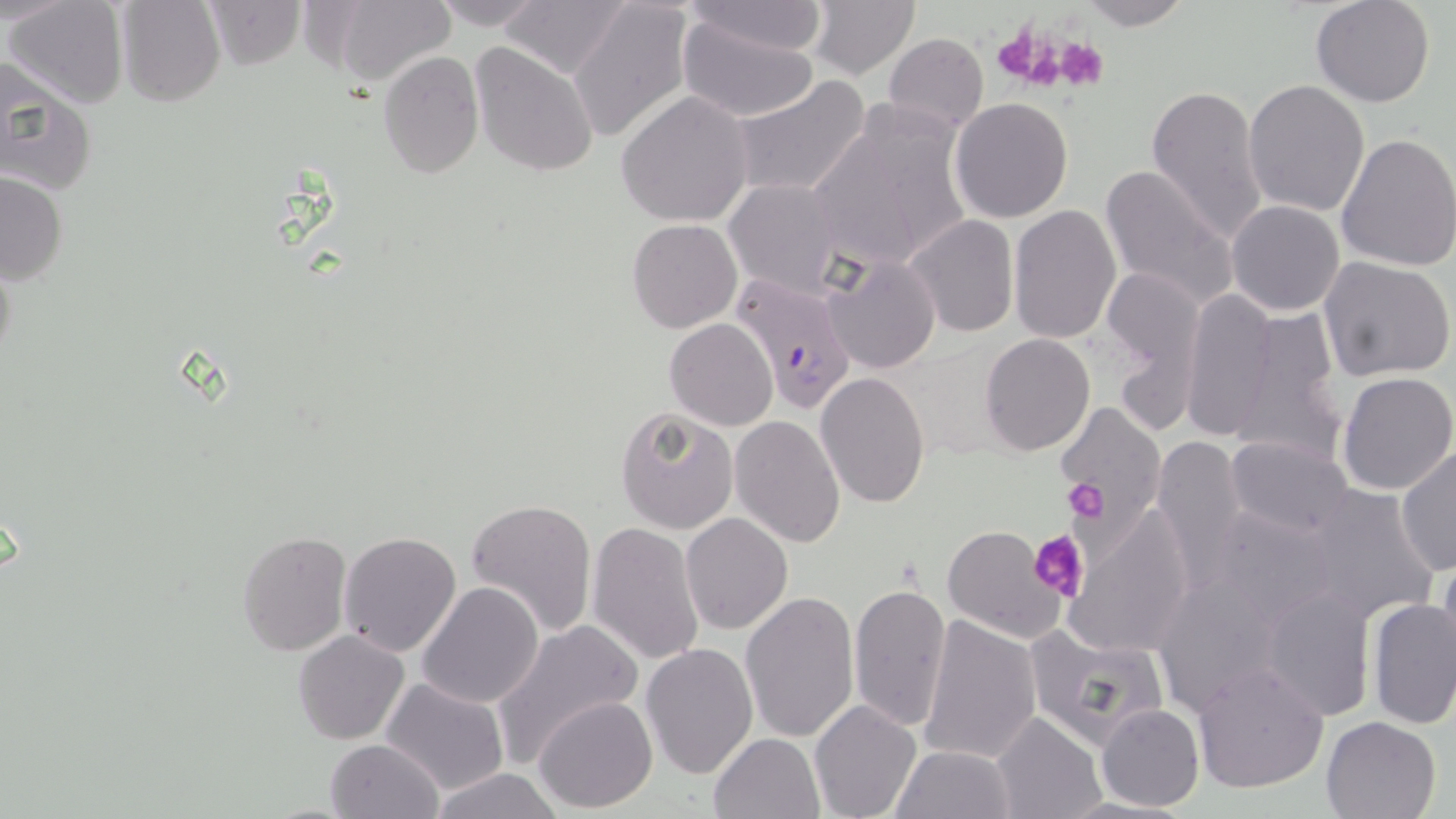

Approximate bounding boxes as (x1,y1)-(x2,y2) corner pairs in pixels. Uninfected red blood cell locations: (4,0)-(130,109), (203,0)-(307,69), (426,0)-(549,30), (500,0)-(631,79), (567,0)-(694,145), (1075,0)-(1195,29), (1310,0)-(1436,108), (115,1)-(225,106), (327,1)-(456,89), (680,1)-(831,57), (807,1)-(919,81), (676,15)-(821,123), (883,33)-(988,134), (471,41)-(599,178), (378,51)-(483,178), (0,57)-(97,196), (731,75)-(871,201), (1242,79)-(1370,217), (1147,82)-(1270,247), (615,92)-(754,228), (951,98)-(1074,223), (804,104)-(974,273), (1334,131)-(1456,272), (1098,162)-(1241,311), (0,170)-(67,284), (723,179)-(846,298), (1226,200)-(1344,316), (1007,204)-(1121,343), (903,214)-(1018,338), (627,219)-(742,332), (823,256)-(940,373), (1319,257)-(1455,381), (1101,265)-(1206,422), (1179,289)-(1278,441), (1224,306)-(1345,465), (665,318)-(778,432), (978,334)-(1097,456), (815,370)-(931,509), (1336,372)-(1456,495), (1057,400)-(1165,526), (614,405)-(741,534), (730,414)-(846,547), (1151,434)-(1250,578), (1226,436)-(1355,539), (1395,448)-(1455,575), (1302,485)-(1439,627), (465,498)-(599,638), (1206,504)-(1343,624), (1062,508)-(1195,657), (680,513)-(793,636), (588,523)-(705,667), (941,526)-(1066,644), (237,530)-(351,655), (338,531)-(463,658), (1435,551)-(1456,664), (1153,574)-(1292,712), (416,581)-(545,707), (849,583)-(951,731), (1263,588)-(1374,720), (739,590)-(860,745), (1366,598)-(1455,732), (917,615)-(1041,765), (491,619)-(641,765), (1025,624)-(1172,750), (294,630)-(409,745), (640,642)-(758,779), (1191,661)-(1330,793), (380,677)-(511,794), (533,695)-(658,811), (810,700)-(922,819), (1097,704)-(1203,813), (991,711)-(1106,819), (1319,716)-(1440,819), (708,731)-(825,819), (326,739)-(443,819), (890,745)-(1019,819), (427,768)-(565,819). Platelet locations: (993,27)-(1051,82), (1010,32)-(1077,92), (1053,35)-(1111,90), (1065,477)-(1108,521), (1028,528)-(1087,603). Plasmodium falciparum-infected red blood cell locations: (732,276)-(857,416). Slide-level diagnosis: Plasmodium falciparum. Thin blood smear. One field of a larger specimen. Light microscopy. Captured at 1000x magnification. May-Grünwald-Giemsa-stained preparation. Image is 1456×819 pixels.